Outline each uninfected red blood cell.
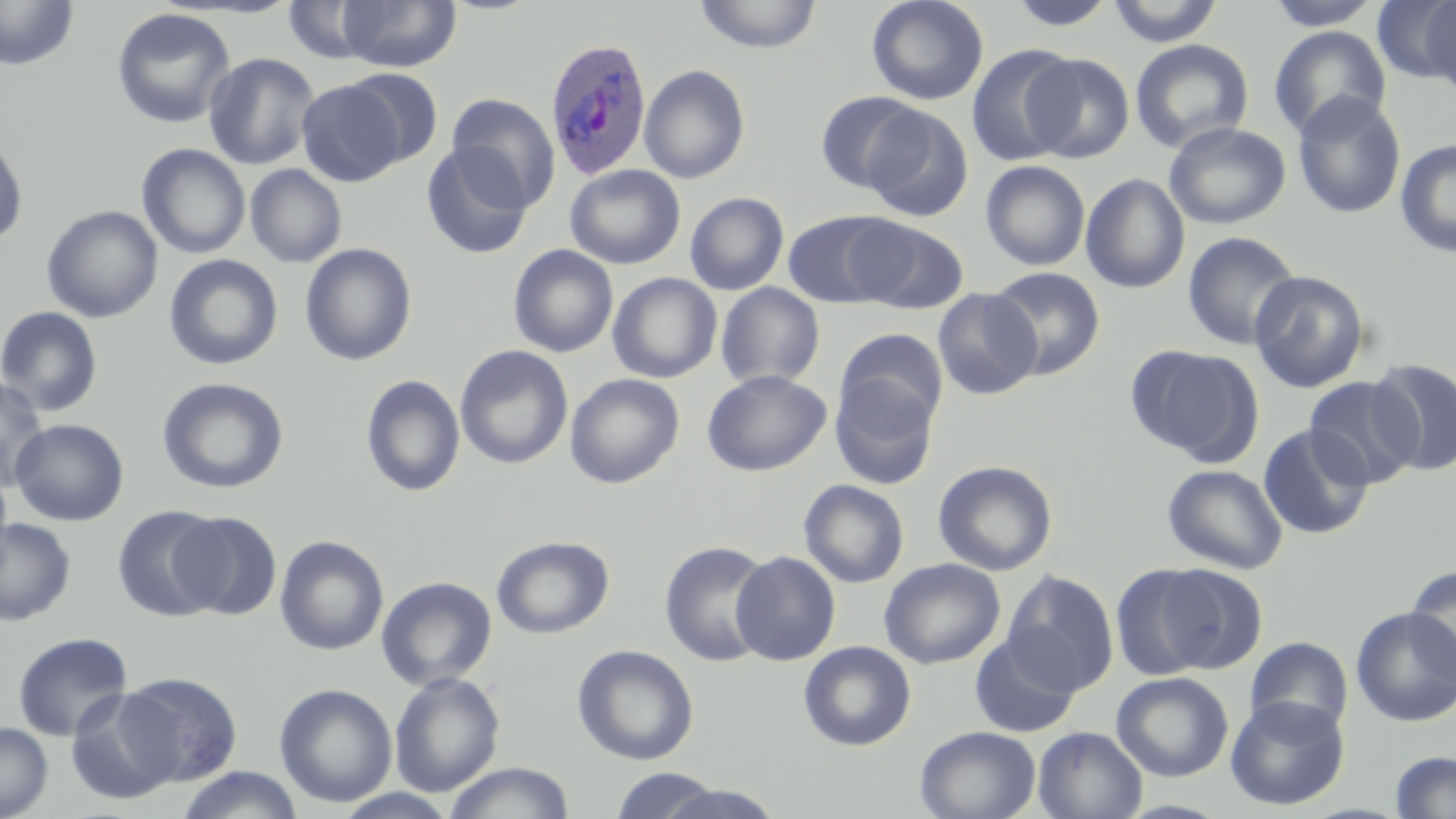
Approximate bounding boxes as [x1, y1, x2, y2] in pixels.
Uninfected red blood cells: [0, 0, 78, 71], [336, 0, 461, 72], [693, 0, 823, 54], [866, 0, 988, 105], [1104, 0, 1224, 47], [1263, 0, 1385, 30], [283, 1, 382, 65], [1006, 1, 1120, 32], [1373, 1, 1456, 84], [1418, 2, 1456, 96], [112, 8, 235, 129], [1268, 25, 1392, 139], [1129, 39, 1254, 154], [966, 45, 1081, 166], [203, 52, 320, 170], [1023, 53, 1134, 163], [639, 64, 750, 184], [341, 68, 444, 168], [296, 79, 408, 186], [815, 90, 925, 193], [1292, 90, 1407, 220], [447, 94, 561, 210], [860, 105, 973, 222], [1164, 122, 1291, 229], [0, 134, 29, 247], [1395, 138, 1456, 258], [136, 143, 251, 259], [421, 143, 533, 260], [981, 160, 1090, 271], [245, 163, 347, 268], [565, 164, 686, 269], [1080, 173, 1190, 293], [685, 192, 789, 295], [41, 205, 163, 323], [782, 211, 902, 308], [849, 217, 968, 314], [1182, 231, 1302, 350], [300, 243, 417, 366], [507, 245, 618, 357], [164, 255, 283, 371], [988, 267, 1105, 380], [1249, 270, 1370, 393], [607, 272, 722, 383], [715, 282, 825, 390], [932, 288, 1042, 401], [0, 306, 104, 417], [835, 328, 947, 429], [1127, 344, 1261, 462], [455, 345, 573, 470], [1369, 358, 1456, 476], [701, 369, 831, 476], [565, 373, 684, 489], [829, 374, 940, 489], [360, 375, 465, 497], [0, 376, 49, 492], [1304, 376, 1422, 489], [156, 377, 289, 495], [3, 417, 89, 628], [9, 418, 129, 526], [1257, 424, 1373, 540], [0, 459, 13, 573], [933, 460, 1058, 576], [1162, 463, 1288, 574], [799, 479, 909, 588], [112, 505, 228, 623], [171, 511, 282, 621], [0, 517, 77, 626], [274, 535, 389, 656], [491, 536, 614, 638], [659, 541, 773, 667], [731, 550, 840, 665], [879, 558, 1005, 669], [1151, 563, 1269, 673], [1405, 564, 1456, 684], [1110, 565, 1216, 679], [1002, 570, 1118, 695], [376, 576, 497, 690], [1351, 606, 1456, 726], [12, 631, 134, 742], [968, 634, 1082, 737], [1245, 636, 1353, 736], [798, 641, 916, 751], [572, 644, 699, 765], [389, 671, 505, 797], [116, 672, 243, 786], [1111, 672, 1234, 781], [274, 682, 398, 808], [66, 688, 184, 804], [1225, 696, 1350, 810], [0, 722, 53, 819], [915, 725, 1041, 819], [1033, 726, 1146, 819], [1389, 751, 1456, 817], [443, 761, 574, 819], [175, 766, 305, 819], [607, 768, 727, 819], [656, 784, 785, 819].

Summary:
  - Plasmodium ovale-infected red blood cell locations: [543, 37, 652, 180]
  - Slide-level diagnosis: Plasmodium ovale
  - Field of view: single
  - Magnification: 1000x
  - Image size: 1456×819 pixels
  - Preparation: thin blood film
  - Modality: optical microscopy
  - Stain: May-Grünwald-Giemsa